Identify the cell.
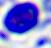

This is a leukocyte.

Photomicrograph. Captured at 400x magnification.